Classify this cell by malaria status.
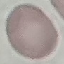
Uninfected.

Acquired by smartphone through the microscope eyepiece. Thin blood smear. Automatically extracted cell patch, resized to 64 × 64 pixels. Giemsa stain.